Report the malaria status of this cell.
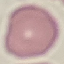

Uninfected.

stain = Giemsa
image type = cell patch, automatically extracted from a larger field of view and resized to 64 × 64 pixels
capture = smartphone camera at the microscope eyepiece
preparation = thin blood film